Name the parasite shown.
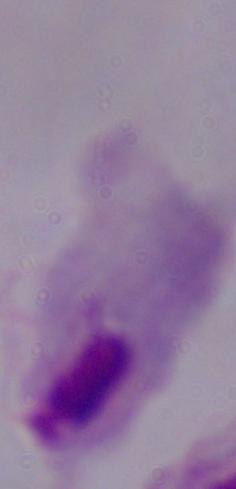
A trichomonad.

Summary:
  - Modality: micrograph
  - Magnification: 1000x